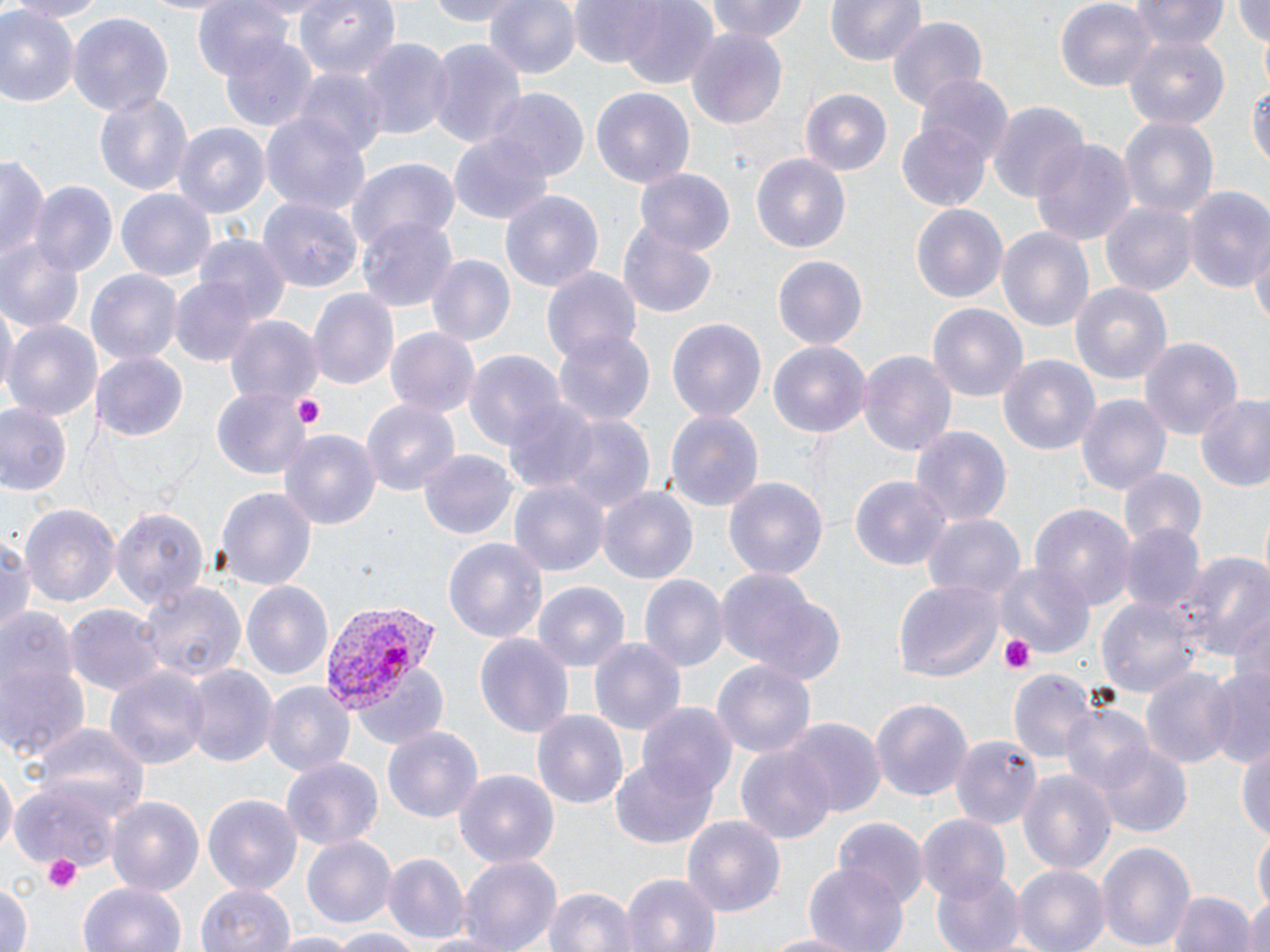

Approximate bounding boxes as named x1/y1/x2/y2 corners in pixels. Uninfected red blood cell locations: (x1=2, y1=0, x2=112, y2=21), (x1=193, y1=0, x2=298, y2=83), (x1=293, y1=0, x2=401, y2=82), (x1=415, y1=0, x2=528, y2=26), (x1=484, y1=0, x2=580, y2=80), (x1=579, y1=0, x2=720, y2=84), (x1=706, y1=0, x2=811, y2=45), (x1=827, y1=0, x2=925, y2=67), (x1=1055, y1=0, x2=1156, y2=89), (x1=1131, y1=0, x2=1227, y2=49), (x1=1232, y1=0, x2=1270, y2=51), (x1=697, y1=4, x2=800, y2=86), (x1=0, y1=7, x2=78, y2=109), (x1=66, y1=12, x2=172, y2=117), (x1=885, y1=16, x2=990, y2=110), (x1=685, y1=26, x2=790, y2=129), (x1=219, y1=32, x2=319, y2=132), (x1=1122, y1=34, x2=1229, y2=130), (x1=421, y1=37, x2=528, y2=150), (x1=358, y1=38, x2=452, y2=143), (x1=294, y1=70, x2=388, y2=162), (x1=915, y1=74, x2=1012, y2=164), (x1=1251, y1=74, x2=1270, y2=180), (x1=591, y1=88, x2=694, y2=193), (x1=486, y1=90, x2=590, y2=184), (x1=94, y1=91, x2=193, y2=197), (x1=801, y1=91, x2=893, y2=179), (x1=988, y1=99, x2=1088, y2=204), (x1=261, y1=111, x2=372, y2=218), (x1=1119, y1=117, x2=1219, y2=225), (x1=897, y1=121, x2=993, y2=213), (x1=175, y1=123, x2=270, y2=221), (x1=450, y1=135, x2=551, y2=224), (x1=1031, y1=139, x2=1135, y2=244), (x1=1, y1=153, x2=50, y2=267), (x1=750, y1=153, x2=851, y2=257), (x1=346, y1=157, x2=460, y2=252), (x1=637, y1=168, x2=735, y2=256), (x1=29, y1=181, x2=118, y2=279), (x1=116, y1=186, x2=216, y2=282), (x1=1182, y1=186, x2=1270, y2=295), (x1=499, y1=190, x2=604, y2=294), (x1=259, y1=196, x2=363, y2=293), (x1=1101, y1=200, x2=1197, y2=298), (x1=910, y1=203, x2=1008, y2=303), (x1=357, y1=216, x2=458, y2=314), (x1=618, y1=221, x2=719, y2=317), (x1=996, y1=226, x2=1096, y2=335), (x1=0, y1=233, x2=86, y2=334), (x1=197, y1=237, x2=292, y2=327), (x1=1248, y1=243, x2=1270, y2=328), (x1=771, y1=252, x2=868, y2=347), (x1=425, y1=255, x2=515, y2=347), (x1=541, y1=264, x2=644, y2=368), (x1=85, y1=269, x2=181, y2=367), (x1=168, y1=273, x2=266, y2=369), (x1=1069, y1=280, x2=1173, y2=385), (x1=307, y1=287, x2=398, y2=391), (x1=0, y1=301, x2=17, y2=402), (x1=929, y1=303, x2=1028, y2=403), (x1=226, y1=317, x2=321, y2=407), (x1=666, y1=317, x2=767, y2=423), (x1=4, y1=321, x2=101, y2=424), (x1=387, y1=327, x2=481, y2=417), (x1=553, y1=329, x2=656, y2=427), (x1=1141, y1=335, x2=1243, y2=441), (x1=768, y1=341, x2=871, y2=441), (x1=857, y1=348, x2=956, y2=459), (x1=464, y1=350, x2=567, y2=454), (x1=997, y1=352, x2=1103, y2=458), (x1=92, y1=354, x2=187, y2=440), (x1=211, y1=388, x2=310, y2=478), (x1=1077, y1=393, x2=1171, y2=499), (x1=1193, y1=393, x2=1270, y2=494), (x1=360, y1=396, x2=460, y2=499), (x1=501, y1=398, x2=600, y2=494), (x1=0, y1=403, x2=73, y2=499), (x1=665, y1=409, x2=765, y2=511), (x1=551, y1=414, x2=656, y2=518), (x1=911, y1=427, x2=1012, y2=525), (x1=280, y1=431, x2=380, y2=530), (x1=420, y1=447, x2=517, y2=540), (x1=1120, y1=464, x2=1206, y2=549), (x1=850, y1=476, x2=948, y2=570), (x1=725, y1=477, x2=829, y2=582), (x1=510, y1=480, x2=608, y2=575), (x1=598, y1=485, x2=700, y2=587), (x1=214, y1=486, x2=317, y2=590), (x1=19, y1=501, x2=119, y2=606), (x1=110, y1=504, x2=210, y2=611), (x1=1031, y1=504, x2=1134, y2=613), (x1=922, y1=513, x2=1025, y2=605), (x1=1121, y1=524, x2=1206, y2=613), (x1=1, y1=535, x2=36, y2=643), (x1=444, y1=537, x2=549, y2=644), (x1=1174, y1=546, x2=1269, y2=663), (x1=994, y1=561, x2=1093, y2=655), (x1=715, y1=568, x2=840, y2=678), (x1=639, y1=574, x2=727, y2=674), (x1=893, y1=579, x2=1002, y2=680), (x1=243, y1=581, x2=333, y2=680), (x1=531, y1=581, x2=630, y2=673), (x1=143, y1=582, x2=245, y2=685), (x1=1098, y1=594, x2=1199, y2=701), (x1=66, y1=606, x2=165, y2=697), (x1=1230, y1=606, x2=1270, y2=696), (x1=3, y1=607, x2=74, y2=702), (x1=475, y1=633, x2=575, y2=738), (x1=588, y1=636, x2=686, y2=737), (x1=0, y1=652, x2=90, y2=765), (x1=714, y1=659, x2=815, y2=763), (x1=104, y1=663, x2=209, y2=773), (x1=351, y1=663, x2=449, y2=751), (x1=1203, y1=665, x2=1270, y2=768), (x1=183, y1=666, x2=276, y2=766), (x1=1140, y1=668, x2=1238, y2=770), (x1=1008, y1=670, x2=1094, y2=766), (x1=262, y1=680, x2=355, y2=776), (x1=869, y1=697, x2=973, y2=802), (x1=639, y1=702, x2=735, y2=799), (x1=1058, y1=703, x2=1155, y2=800), (x1=533, y1=708, x2=628, y2=812), (x1=786, y1=718, x2=884, y2=816), (x1=33, y1=720, x2=149, y2=820), (x1=383, y1=726, x2=482, y2=822), (x1=950, y1=735, x2=1041, y2=829), (x1=736, y1=742, x2=836, y2=843), (x1=1237, y1=742, x2=1270, y2=847), (x1=1096, y1=743, x2=1190, y2=839), (x1=610, y1=755, x2=718, y2=848), (x1=281, y1=757, x2=384, y2=853), (x1=0, y1=764, x2=17, y2=856), (x1=453, y1=769, x2=562, y2=869), (x1=1019, y1=769, x2=1117, y2=879), (x1=13, y1=773, x2=131, y2=869), (x1=202, y1=793, x2=303, y2=893), (x1=105, y1=794, x2=205, y2=896), (x1=683, y1=814, x2=785, y2=920), (x1=916, y1=814, x2=1011, y2=904), (x1=836, y1=817, x2=928, y2=910), (x1=1253, y1=829, x2=1269, y2=917), (x1=302, y1=834, x2=396, y2=930), (x1=1095, y1=839, x2=1197, y2=950), (x1=383, y1=853, x2=468, y2=944), (x1=456, y1=854, x2=562, y2=952), (x1=802, y1=862, x2=910, y2=952), (x1=1013, y1=864, x2=1109, y2=952), (x1=932, y1=869, x2=1024, y2=952), (x1=621, y1=873, x2=721, y2=952), (x1=79, y1=879, x2=186, y2=952), (x1=0, y1=880, x2=32, y2=952), (x1=197, y1=881, x2=291, y2=952), (x1=1166, y1=887, x2=1258, y2=952), (x1=544, y1=888, x2=634, y2=952), (x1=1242, y1=891, x2=1270, y2=952), (x1=329, y1=928, x2=424, y2=952), (x1=406, y1=929, x2=516, y2=951), (x1=756, y1=930, x2=865, y2=952), (x1=271, y1=933, x2=356, y2=952). Platelet locations: (x1=291, y1=394, x2=327, y2=430), (x1=1001, y1=633, x2=1037, y2=674), (x1=42, y1=854, x2=84, y2=894). Plasmodium vivax-infected red blood cell locations: (x1=325, y1=602, x2=436, y2=710). Slide-level diagnosis: Plasmodium vivax. May-Grünwald-Giemsa-stained preparation. Image is 1270×952 pixels. Thin blood film. Optical microscopy. One field of a larger specimen. Captured at 1000x magnification.